Name the parasite shown.
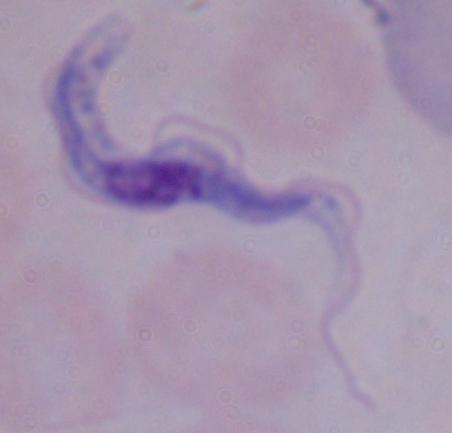

A trypanosome.

Summary:
  - Modality: photomicrograph
  - Magnification: 1000x